Give the extent of all uninfected red blood cells.
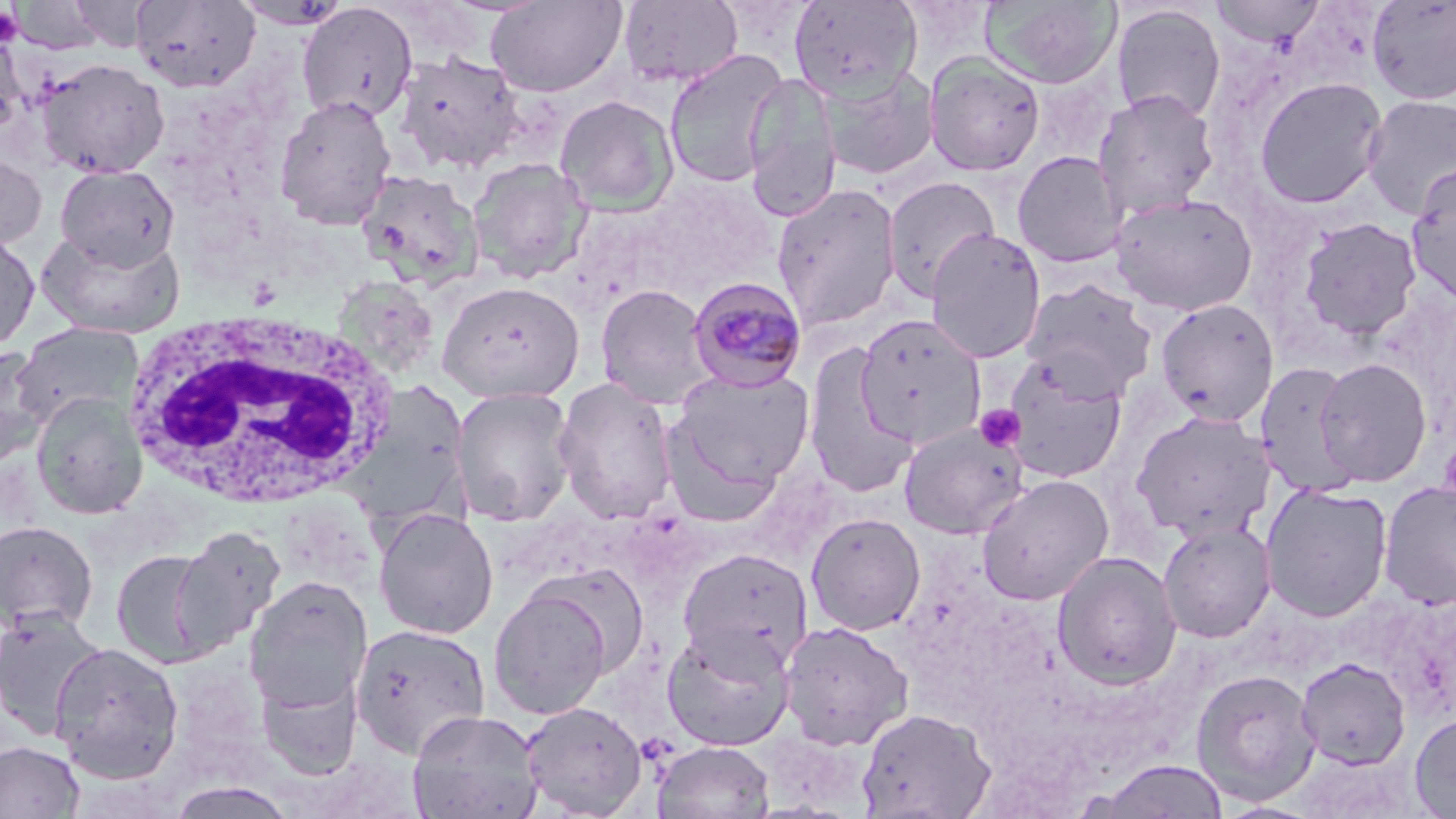

Approximate bounding boxes as [x1, y1, x2, y2] in pixels.
Uninfected red blood cells: [486, 0, 626, 97], [618, 0, 745, 88], [788, 0, 924, 100], [981, 0, 1121, 89], [1366, 0, 1456, 106], [10, 1, 104, 54], [68, 1, 153, 51], [131, 1, 261, 92], [233, 1, 353, 30], [1209, 1, 1324, 47], [297, 2, 419, 123], [1111, 4, 1226, 123], [0, 29, 27, 136], [663, 49, 789, 189], [393, 50, 525, 175], [923, 52, 1046, 176], [35, 57, 170, 179], [818, 66, 940, 180], [743, 72, 841, 222], [1254, 76, 1388, 209], [1093, 89, 1219, 220], [273, 94, 398, 229], [554, 94, 679, 216], [1361, 95, 1456, 220], [1012, 150, 1128, 268], [0, 153, 46, 253], [466, 157, 593, 283], [54, 164, 180, 271], [1405, 164, 1456, 305], [356, 169, 485, 293], [881, 175, 1001, 302], [770, 183, 902, 331], [1109, 191, 1258, 317], [1298, 217, 1422, 341], [0, 228, 40, 353], [36, 228, 186, 338], [926, 228, 1047, 363], [330, 274, 440, 380], [1020, 278, 1158, 400], [437, 280, 584, 404], [594, 283, 716, 409], [1154, 298, 1280, 427], [854, 315, 987, 450], [12, 321, 144, 429], [802, 340, 918, 499], [0, 346, 49, 466], [1002, 354, 1128, 483], [1313, 357, 1432, 487], [1254, 360, 1363, 497], [672, 368, 815, 489], [553, 377, 678, 524], [451, 386, 579, 527], [30, 391, 148, 519], [1130, 409, 1277, 542], [899, 421, 1028, 539], [663, 429, 782, 529], [976, 474, 1115, 606], [1378, 480, 1456, 611], [1259, 483, 1394, 621], [372, 507, 500, 640], [805, 513, 926, 635], [0, 519, 99, 634], [1157, 520, 1275, 643], [169, 525, 286, 654], [677, 548, 813, 670], [111, 549, 218, 668], [1051, 551, 1182, 690], [533, 562, 651, 679], [243, 576, 372, 711], [489, 586, 612, 720], [0, 607, 110, 739], [779, 620, 914, 750], [349, 623, 492, 759], [661, 623, 796, 752], [48, 642, 185, 783], [1296, 657, 1411, 770], [255, 663, 366, 780], [1191, 667, 1322, 806], [520, 701, 649, 818], [856, 708, 996, 818], [406, 709, 545, 819], [1409, 712, 1456, 818], [0, 740, 85, 819], [652, 740, 775, 819], [1093, 759, 1230, 819], [165, 781, 298, 819].

Platelet locations: [0, 6, 24, 46], [975, 405, 1025, 452]. Plasmodium malariae-infected red blood cell locations: [687, 276, 808, 392]. White blood cell locations: [120, 309, 408, 513]. Slide-level diagnosis: Plasmodium malariae. Image is 1456×819 pixels. Thin blood film. One field of a larger specimen. May-Grünwald-Giemsa-stained preparation. Optical microscopy. 1000x magnification.